Give the position of every Plasmodium parasite.
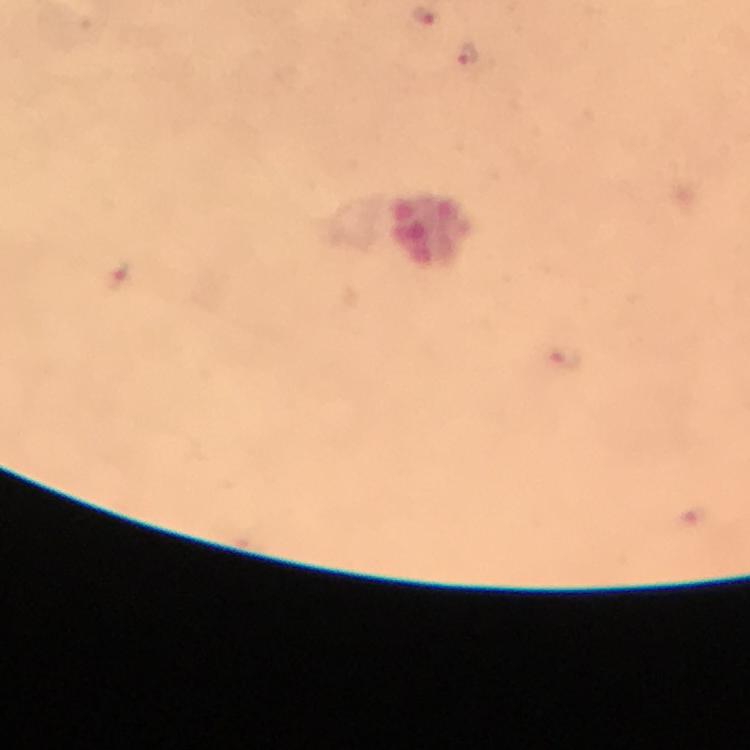

Approximate centers as (x, y) in pixels.
Plasmodium parasites: (424, 16), (468, 54), (121, 275), (565, 357).

Summary:
  - Magnification: 100x
  - Stain: Giemsa
  - Context: from a malaria diagnostic workup
  - Cropped from: one field of view
  - Preparation: thick blood film
  - Capture: smartphone mounted on the microscope
  - Image size: 750×750 pixels
  - Immersion oil: used